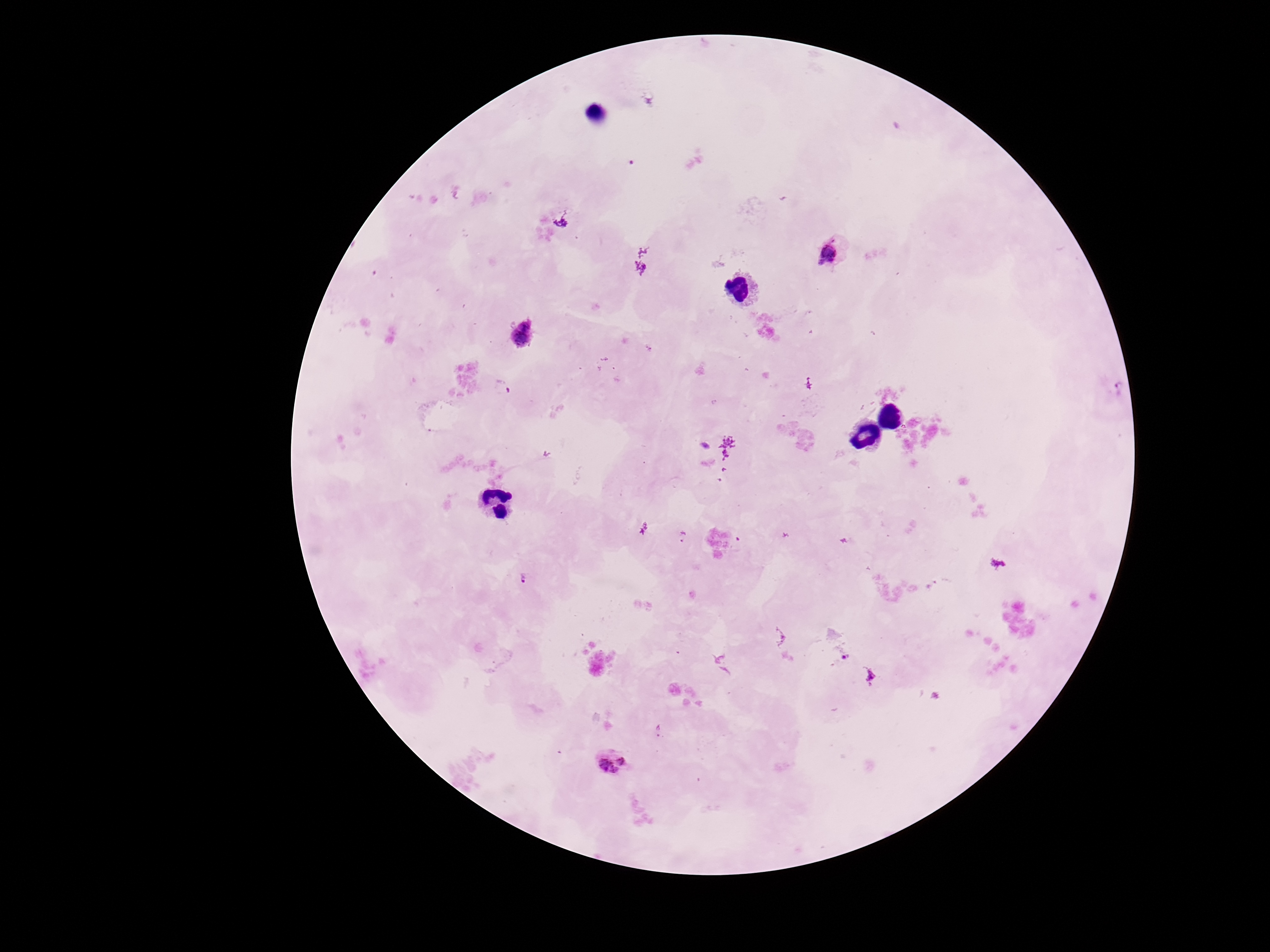

Approximate object centers, in pixels from the top-left corner.
Summary:
  - Plasmodium parasite locations: (x=832, y=254), (x=522, y=337), (x=683, y=536), (x=523, y=577), (x=871, y=676), (x=659, y=731), (x=611, y=762)
  - Image size: 1270×952 pixels
  - Preparation: thick blood film
  - Magnification: 100x
  - Capture: smartphone camera through the microscope eyepiece
  - Field of view: single
  - Patient malaria status: positive
  - Stain: Giemsa